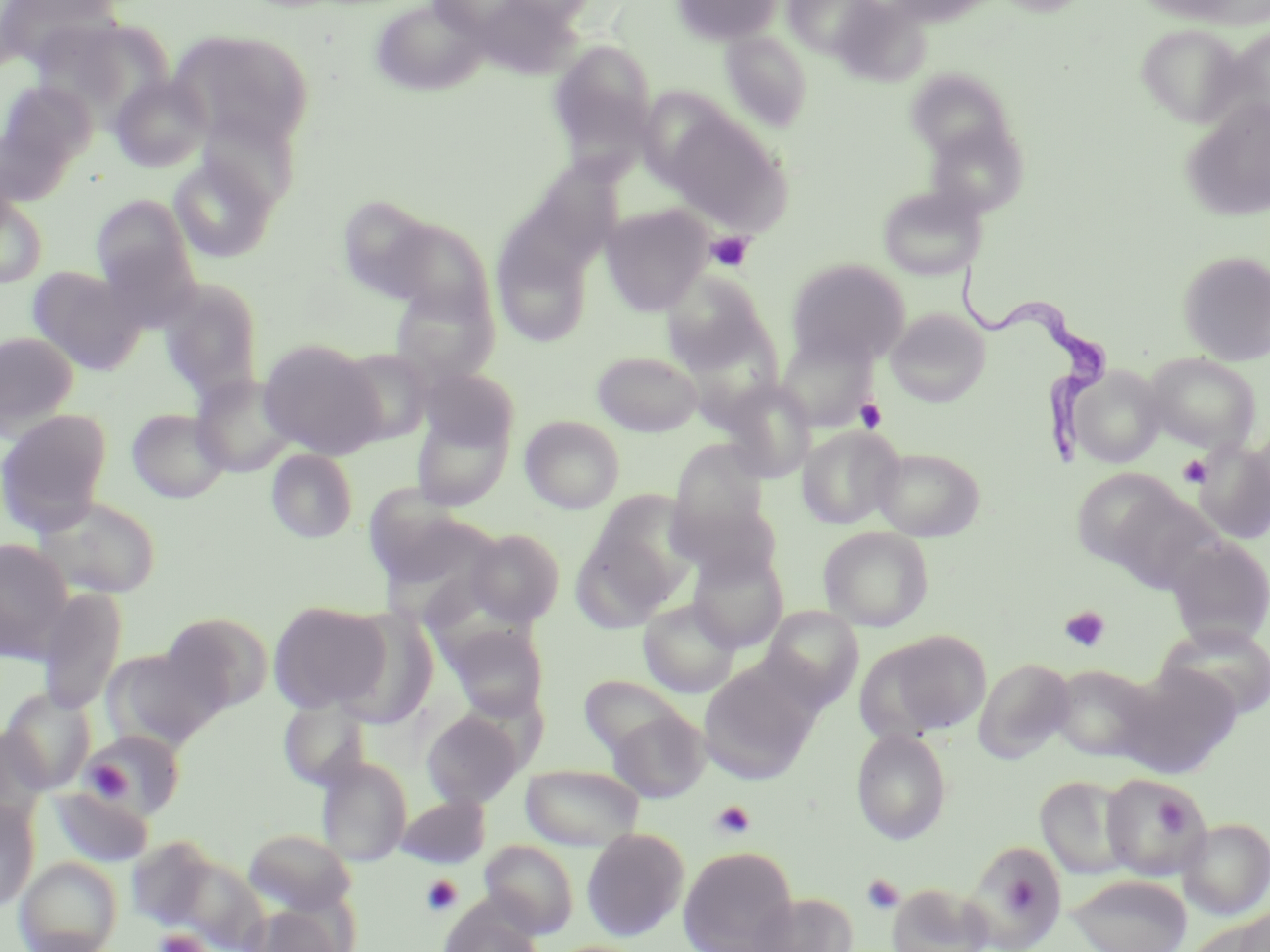
Approximate bounding boxes as [x1, y1, x2, y2] in pixels. Uninfected red blood cell locations: [0, 0, 123, 75], [369, 0, 490, 97], [498, 0, 601, 25], [671, 0, 784, 46], [783, 0, 881, 58], [992, 0, 1092, 16], [1131, 0, 1259, 25], [1135, 25, 1245, 127], [1220, 26, 1270, 127], [168, 28, 315, 149], [720, 30, 813, 132], [547, 38, 658, 164], [904, 70, 1015, 161], [109, 74, 212, 172], [0, 80, 97, 173], [1180, 97, 1270, 221], [661, 111, 792, 234], [197, 112, 297, 209], [925, 120, 1029, 217], [169, 154, 279, 263], [527, 163, 618, 253], [877, 185, 986, 280], [90, 194, 196, 296], [0, 195, 48, 287], [338, 198, 429, 295], [600, 204, 712, 315], [381, 217, 496, 322], [493, 238, 592, 347], [1178, 250, 1270, 366], [786, 258, 910, 367], [27, 266, 145, 372], [660, 269, 776, 381], [158, 278, 264, 401], [390, 281, 500, 385], [885, 308, 991, 407], [0, 331, 80, 434], [775, 336, 875, 432], [257, 338, 385, 458], [335, 348, 435, 446], [592, 351, 703, 436], [1143, 353, 1261, 453], [1068, 365, 1167, 468], [418, 367, 521, 452], [191, 374, 300, 477], [719, 380, 816, 483], [126, 408, 231, 503], [0, 409, 113, 533], [411, 409, 513, 512], [520, 415, 625, 514], [797, 426, 903, 529], [669, 439, 770, 540], [1191, 439, 1270, 544], [678, 441, 779, 643], [872, 447, 986, 541], [266, 449, 359, 543], [1071, 467, 1187, 571], [1098, 483, 1222, 594], [589, 490, 699, 590], [668, 493, 784, 583], [32, 495, 163, 600], [374, 511, 508, 630], [818, 527, 934, 631], [465, 528, 566, 626], [570, 528, 680, 632], [1165, 536, 1270, 647], [0, 538, 75, 662], [687, 548, 789, 652], [37, 587, 127, 715], [638, 599, 741, 698], [268, 600, 392, 714], [761, 606, 863, 709], [161, 611, 272, 710], [329, 611, 438, 728], [443, 622, 549, 719], [1157, 623, 1270, 722], [874, 630, 993, 738], [101, 646, 223, 750], [975, 658, 1074, 762], [697, 660, 822, 783], [1113, 664, 1241, 778], [1048, 665, 1159, 762], [579, 674, 688, 758], [0, 687, 96, 794], [278, 697, 371, 790], [420, 707, 527, 809], [608, 709, 710, 803], [1, 726, 50, 831], [851, 728, 952, 845], [79, 729, 186, 821], [317, 757, 412, 866], [520, 764, 646, 850], [1101, 774, 1208, 881], [1035, 775, 1135, 879], [49, 787, 154, 867], [397, 794, 490, 869], [0, 800, 39, 912], [1180, 816, 1270, 920], [244, 828, 356, 915], [581, 828, 689, 941], [480, 840, 579, 939], [963, 841, 1068, 951], [678, 846, 798, 951], [148, 847, 268, 950], [15, 856, 123, 952], [1067, 873, 1191, 952], [887, 883, 992, 952], [747, 891, 857, 952], [439, 898, 544, 952], [245, 903, 348, 952], [1233, 907, 1270, 952]. Platelet locations: [706, 232, 754, 272], [855, 398, 887, 432], [1178, 455, 1212, 488], [1060, 606, 1110, 653], [91, 754, 131, 802], [1155, 797, 1190, 836], [712, 800, 755, 839], [861, 874, 904, 915], [422, 875, 462, 917], [1011, 880, 1044, 915], [154, 929, 209, 952]. Trypanosoma brucei locations: [953, 258, 1116, 464]. Slide-level diagnosis: Trypanosoma brucei. Image is 1270×952 pixels. May-Grünwald-Giemsa-stained preparation. One field of a larger specimen. Captured at 1000x magnification. Thin blood film. Light microscopy.